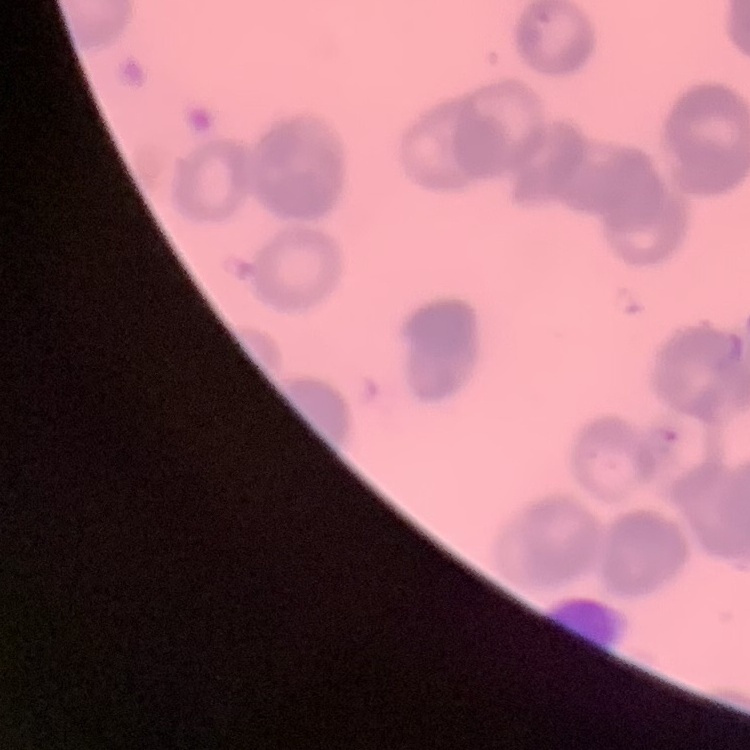

Summary:
  - Red blood cell morphology: rouleaux formation
  - Preparation: thin blood film
  - Image type: square crop of a larger photomicrograph
  - Stain: Field's or Giemsa